Report the malaria status of this cell.
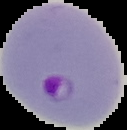

It is parasitized.

image size = 127×130 pixels
preparation = thin blood film
image type = segmented cell region on a black background